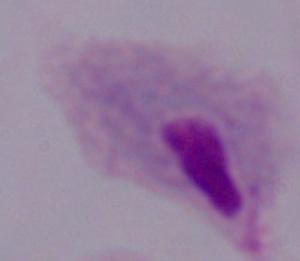 A trichomonad is shown. 1000x magnification. Photomicrograph.